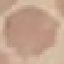
Summary:
  - Malaria status: uninfected
  - Image type: cell patch, automatically extracted from a larger field of view and resized to 64 × 64 pixels
  - Preparation: thin smear
  - Capture: smartphone through the microscope eyepiece
  - Stain: Giemsa